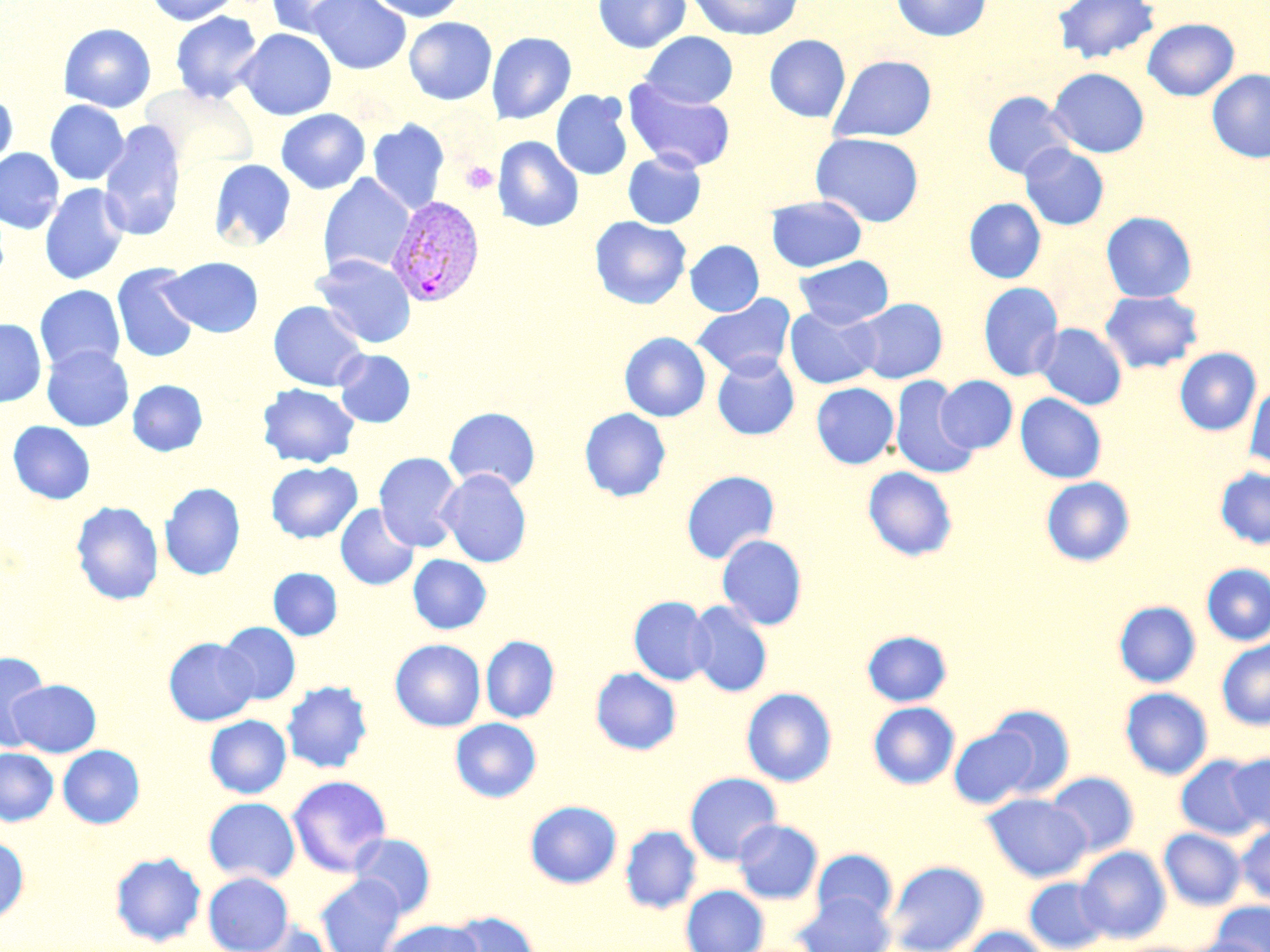 Approximate bounding boxes as [x1, y1, x2, y2] in pixels. Plasmodium vivax-infected red blood cell locations: [387, 194, 486, 307]. Uninfected red blood cell locations: [146, 0, 240, 25], [307, 0, 411, 74], [367, 0, 467, 22], [593, 0, 690, 53], [687, 0, 803, 40], [891, 0, 991, 41], [1051, 0, 1161, 64], [268, 1, 364, 37], [170, 11, 263, 103], [404, 17, 497, 105], [1142, 18, 1239, 100], [58, 23, 156, 113], [236, 28, 337, 120], [486, 31, 576, 124], [640, 31, 738, 108], [764, 34, 851, 122], [829, 54, 937, 142], [1048, 68, 1149, 157], [1208, 70, 1270, 163], [623, 78, 736, 174], [551, 90, 633, 181], [982, 91, 1075, 179], [0, 92, 18, 173], [45, 100, 129, 185], [276, 109, 370, 194], [98, 119, 186, 242], [367, 119, 449, 214], [811, 132, 924, 227], [493, 136, 583, 232], [1019, 144, 1109, 230], [0, 148, 64, 234], [623, 151, 706, 229], [209, 159, 297, 251], [319, 174, 415, 277], [39, 183, 130, 285], [767, 195, 867, 272], [964, 198, 1046, 283], [1101, 211, 1197, 302], [589, 216, 691, 309], [685, 240, 764, 316], [311, 254, 416, 348], [794, 256, 893, 329], [161, 257, 263, 337], [112, 262, 199, 363], [978, 282, 1063, 382], [34, 285, 125, 374], [1100, 290, 1204, 374], [691, 293, 796, 379], [852, 298, 948, 384], [268, 300, 370, 391], [785, 306, 881, 389], [0, 319, 46, 407], [1035, 323, 1127, 409], [619, 332, 711, 422], [42, 345, 134, 431], [1174, 347, 1261, 435], [334, 349, 415, 428], [711, 353, 799, 440], [936, 375, 1018, 453], [890, 376, 979, 479], [127, 379, 207, 455], [1245, 379, 1270, 471], [257, 383, 359, 468], [811, 383, 899, 469], [1015, 393, 1107, 483], [444, 407, 540, 492], [579, 408, 671, 501], [8, 421, 96, 504], [374, 452, 463, 552], [266, 460, 362, 543], [863, 467, 957, 561], [1215, 467, 1270, 549], [437, 469, 531, 567], [681, 470, 779, 564], [1041, 476, 1135, 566], [160, 482, 245, 580], [71, 501, 163, 605], [336, 504, 419, 590], [717, 534, 807, 630], [408, 554, 491, 634], [1201, 563, 1270, 646], [268, 568, 342, 640], [629, 596, 714, 685], [687, 601, 773, 697], [1113, 601, 1201, 687], [218, 622, 301, 705], [862, 630, 952, 706], [480, 636, 559, 723], [165, 637, 258, 726], [390, 639, 485, 731], [1217, 640, 1270, 730], [0, 651, 51, 750], [590, 667, 682, 755], [8, 679, 101, 757], [281, 680, 373, 773], [741, 687, 837, 786], [1120, 688, 1212, 779], [868, 702, 959, 789], [982, 704, 1077, 798], [204, 715, 291, 798], [450, 717, 542, 802], [948, 724, 1042, 809], [58, 744, 145, 828], [0, 748, 58, 826], [1224, 752, 1270, 834], [1177, 755, 1265, 840], [1045, 771, 1139, 857], [684, 772, 782, 865], [287, 774, 392, 876], [982, 793, 1091, 881], [203, 797, 300, 884], [525, 800, 622, 888], [733, 819, 822, 904], [620, 825, 701, 913], [1236, 825, 1270, 905], [1159, 828, 1246, 909], [350, 833, 436, 918], [0, 837, 29, 923], [1076, 846, 1171, 943], [812, 849, 897, 926], [110, 851, 206, 946], [886, 860, 989, 952], [203, 872, 294, 952], [316, 874, 406, 952], [1024, 877, 1110, 952], [680, 885, 769, 952], [794, 891, 894, 952], [1211, 901, 1270, 952], [446, 910, 539, 952], [380, 919, 484, 952], [240, 920, 331, 952], [958, 926, 1050, 952], [1182, 937, 1267, 952]. Platelet locations: [460, 161, 498, 194]. Slide-level diagnosis: Plasmodium vivax. Image is 1270×952 pixels. Single field of view. Light microscopy. 1000x magnification. Thin blood film. May-Grünwald-Giemsa-stained preparation.